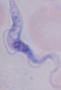

Summary:
  - Magnification: 1000x
  - Identification: trypanosome
  - Modality: photomicrograph